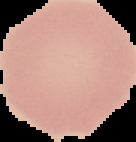

image size = 136×142 pixels
image type = segmented cell region with the area outside set to black
preparation = thin blood film
malaria status = uninfected